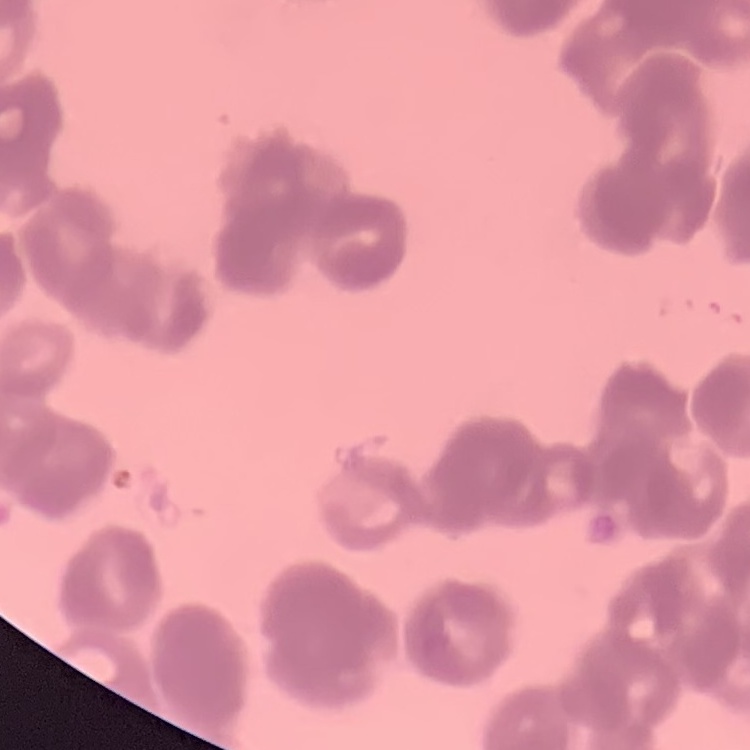 The red blood cells exhibit rouleaux formation. One tile cut from a larger photomicrograph. Thin blood smear. Stained with either Field's or Giemsa.